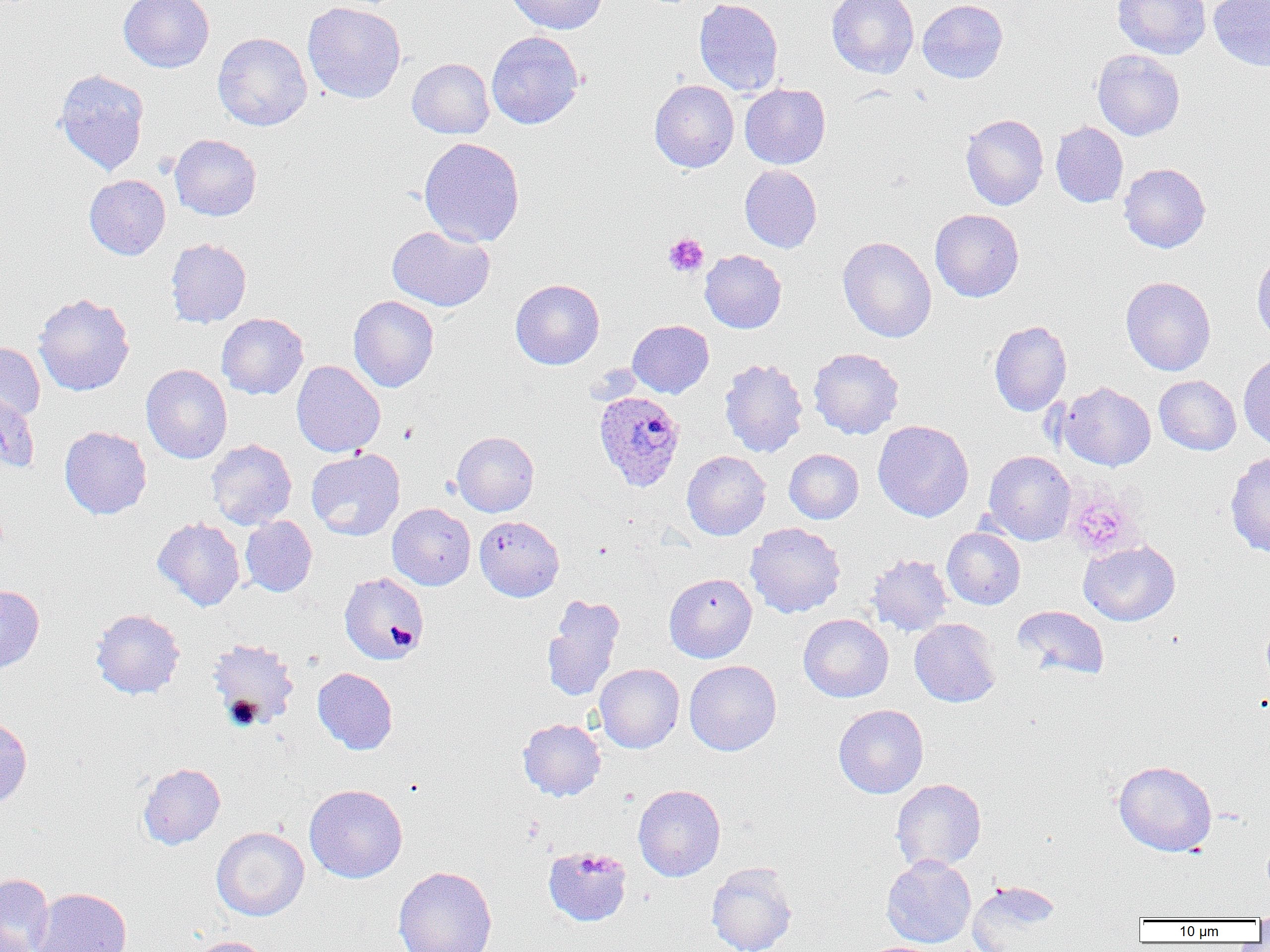
Summary:
  - Coordinate format: approximate bounding boxes as (x1, y1, x2, y2) in pixels
  - Plasmodium ovale-infected red blood cell locations: (595, 396, 687, 497)
  - Uninfected red blood cell locations: (118, 0, 214, 72), (506, 0, 608, 34), (694, 0, 784, 96), (826, 0, 919, 78), (917, 0, 1008, 83), (1112, 0, 1211, 59), (1208, 0, 1270, 71), (302, 1, 406, 103), (486, 31, 584, 129), (212, 32, 312, 131), (1092, 50, 1185, 141), (407, 58, 495, 138), (54, 69, 150, 175), (649, 80, 739, 172), (740, 83, 830, 169), (961, 113, 1049, 210), (1050, 121, 1128, 207), (170, 134, 262, 221), (418, 137, 525, 247), (1119, 163, 1210, 253), (740, 164, 822, 252), (84, 174, 170, 260), (930, 209, 1024, 302), (387, 226, 495, 311), (838, 237, 936, 343), (166, 239, 251, 328), (1251, 248, 1270, 349), (700, 249, 787, 333), (1121, 277, 1216, 376), (510, 279, 605, 369), (33, 293, 135, 396), (348, 295, 439, 392), (217, 313, 308, 399), (627, 319, 714, 398), (989, 320, 1072, 416), (0, 342, 45, 422), (808, 347, 904, 439), (1238, 354, 1270, 451), (719, 357, 808, 457), (291, 360, 385, 457), (141, 364, 232, 463), (1154, 375, 1241, 455), (1058, 381, 1156, 471), (873, 420, 974, 521), (59, 426, 152, 519), (452, 431, 539, 516), (206, 438, 296, 530), (306, 448, 405, 540), (784, 449, 863, 523), (681, 450, 771, 540), (983, 450, 1076, 545), (1225, 451, 1270, 558), (387, 503, 475, 590), (240, 516, 317, 596), (474, 516, 564, 600), (152, 518, 245, 611), (745, 522, 846, 618), (942, 527, 1025, 609), (1079, 540, 1180, 626), (867, 554, 953, 636), (664, 572, 757, 662), (339, 573, 429, 664), (0, 584, 44, 673), (542, 594, 626, 702), (1013, 605, 1109, 681), (91, 609, 185, 699), (798, 614, 893, 702), (909, 618, 1001, 707), (207, 638, 300, 729), (684, 660, 781, 755), (594, 663, 684, 753), (312, 667, 397, 754), (833, 704, 928, 798), (0, 715, 32, 810), (518, 718, 606, 801), (1113, 760, 1217, 856), (138, 762, 225, 849), (891, 778, 987, 873), (304, 784, 407, 883), (633, 784, 725, 881), (211, 827, 309, 921), (543, 847, 632, 927), (882, 855, 976, 948), (706, 862, 797, 952), (393, 865, 497, 952), (0, 873, 54, 952), (966, 881, 1063, 952), (34, 887, 132, 952), (188, 936, 272, 952)
  - Platelet locations: (663, 232, 709, 276), (1064, 487, 1144, 560)
  - Slide-level diagnosis: Plasmodium ovale
  - Image size: 1270×952 pixels
  - Modality: optical microscopy
  - Magnification: 1000x
  - Field of view: one of a larger specimen
  - Preparation: thin blood film